Report the malaria status of this cell.
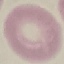

Uninfected.

Summary:
  - Image type: automatically extracted cell patch, resized to 64 × 64 pixels
  - Preparation: thin smear
  - Stain: Giemsa
  - Capture: smartphone through the microscope eyepiece